Locate every Plasmodium parasite.
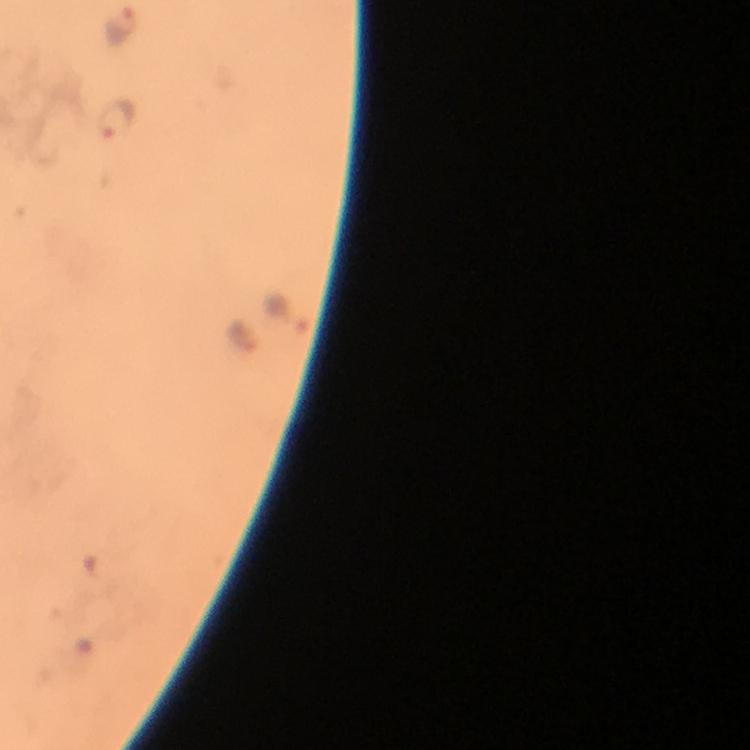

Approximate centers as {x, y} in pixels.
Plasmodium parasites: {121, 24}, {117, 118}, {288, 311}.

Summary:
  - Capture: smartphone mounted on the microscope
  - Cropped from: one field of view
  - Image size: 750×750 pixels
  - Context: from a diagnostic examination for malaria
  - Preparation: thick smear
  - Stain: Giemsa
  - Magnification: 100x
  - Immersion oil: applied